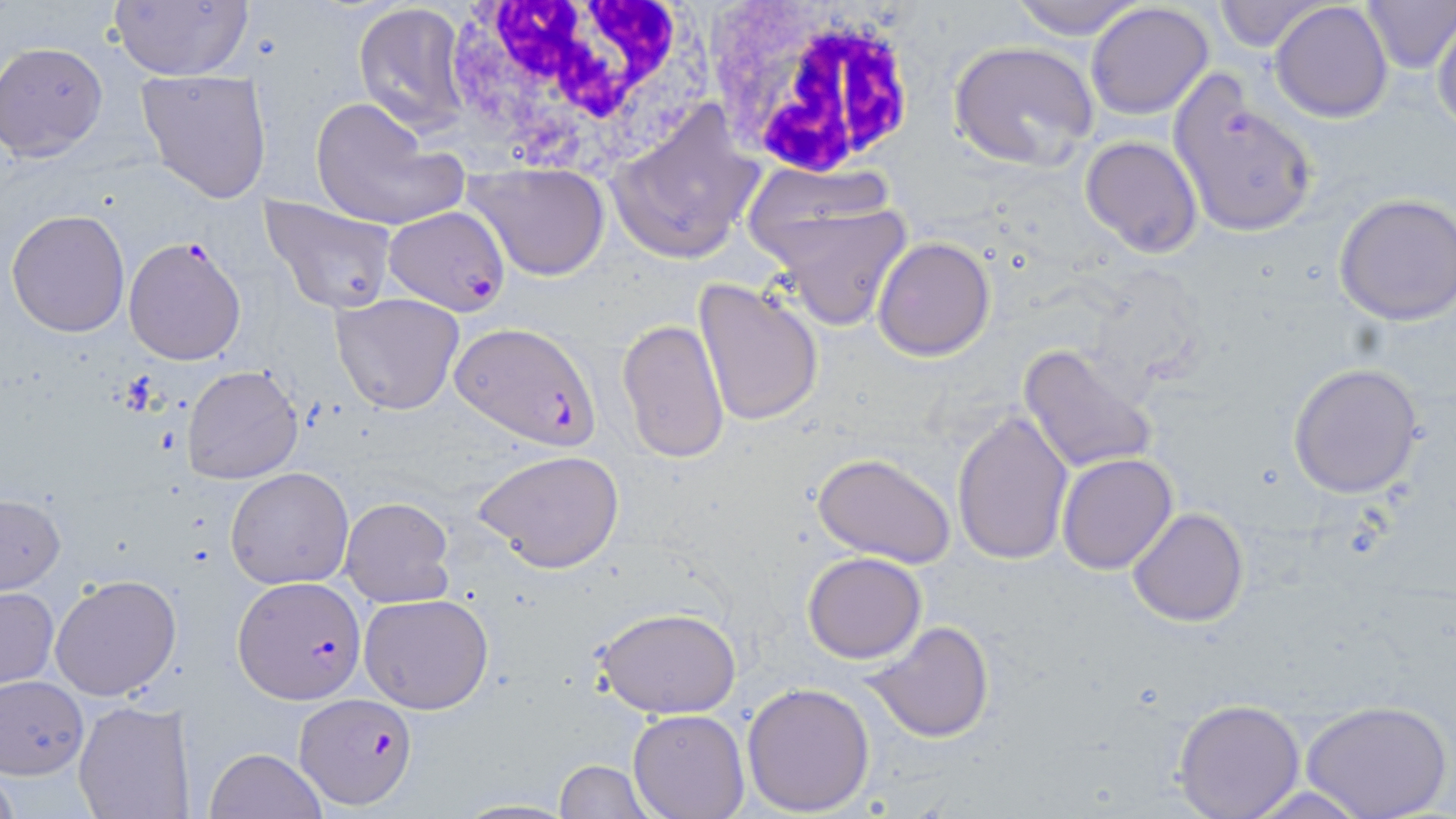
slide_level_diagnosis: Plasmodium falciparum
stain: May-Grünwald-Giemsa
uninfected_red_blood_cell_locations: 'approximate bounding boxes as named x1/y1/x2/y2 corners in pixels: (x1=105, y1=0, x2=255, y2=81), (x1=1009, y1=0, x2=1148, y2=40), (x1=1213, y1=0, x2=1326, y2=52), (x1=1362, y1=0, x2=1456, y2=73), (x1=1270, y1=1, x2=1394, y2=123), (x1=1085, y1=2, x2=1215, y2=121), (x1=353, y1=4, x2=468, y2=130), (x1=1430, y1=20, x2=1455, y2=134), (x1=949, y1=40, x2=1101, y2=169), (x1=1, y1=42, x2=108, y2=160), (x1=135, y1=69, x2=273, y2=203), (x1=1165, y1=70, x2=1323, y2=240), (x1=309, y1=96, x2=466, y2=233), (x1=606, y1=99, x2=765, y2=266), (x1=1079, y1=136, x2=1203, y2=257), (x1=466, y1=163, x2=611, y2=280), (x1=741, y1=163, x2=900, y2=264), (x1=1333, y1=192, x2=1456, y2=325), (x1=260, y1=194, x2=397, y2=315), (x1=766, y1=203, x2=913, y2=332), (x1=7, y1=209, x2=128, y2=337), (x1=872, y1=237, x2=995, y2=360), (x1=691, y1=279, x2=823, y2=430), (x1=330, y1=293, x2=465, y2=415), (x1=617, y1=318, x2=730, y2=464), (x1=1018, y1=342, x2=1159, y2=476), (x1=1285, y1=364, x2=1425, y2=500), (x1=181, y1=365, x2=303, y2=485), (x1=951, y1=410, x2=1074, y2=567), (x1=473, y1=449, x2=625, y2=573), (x1=1058, y1=453, x2=1177, y2=574), (x1=812, y1=454, x2=955, y2=567), (x1=225, y1=466, x2=354, y2=589), (x1=0, y1=494, x2=65, y2=593), (x1=339, y1=496, x2=454, y2=608), (x1=1127, y1=507, x2=1250, y2=628), (x1=802, y1=551, x2=927, y2=663), (x1=49, y1=573, x2=183, y2=702), (x1=1, y1=586, x2=58, y2=687), (x1=358, y1=593, x2=496, y2=714), (x1=594, y1=607, x2=743, y2=719), (x1=864, y1=620, x2=996, y2=744), (x1=1, y1=675, x2=88, y2=776), (x1=742, y1=681, x2=876, y2=815), (x1=1172, y1=697, x2=1306, y2=819), (x1=73, y1=699, x2=193, y2=819), (x1=1303, y1=699, x2=1451, y2=819), (x1=628, y1=710, x2=749, y2=818), (x1=206, y1=746, x2=328, y2=819), (x1=555, y1=759, x2=651, y2=818), (x1=452, y1=799, x2=578, y2=818)'
image_size: 1456×819 pixels
preparation: thin blood smear
modality: light microscopy
plasmodium_falciparum_infected_red_blood_cell_locations: 'approximate bounding boxes as named x1/y1/x2/y2 corners in pixels: (x1=385, y1=205, x2=510, y2=316), (x1=122, y1=236, x2=248, y2=366), (x1=451, y1=321, x2=603, y2=450), (x1=231, y1=575, x2=367, y2=703), (x1=295, y1=693, x2=416, y2=809)'
white_blood_cell_locations: 'approximate bounding boxes as named x1/y1/x2/y2 corners in pixels: (x1=442, y1=0, x2=707, y2=171), (x1=708, y1=4, x2=923, y2=184)'
field_of_view: single
magnification: 1000x